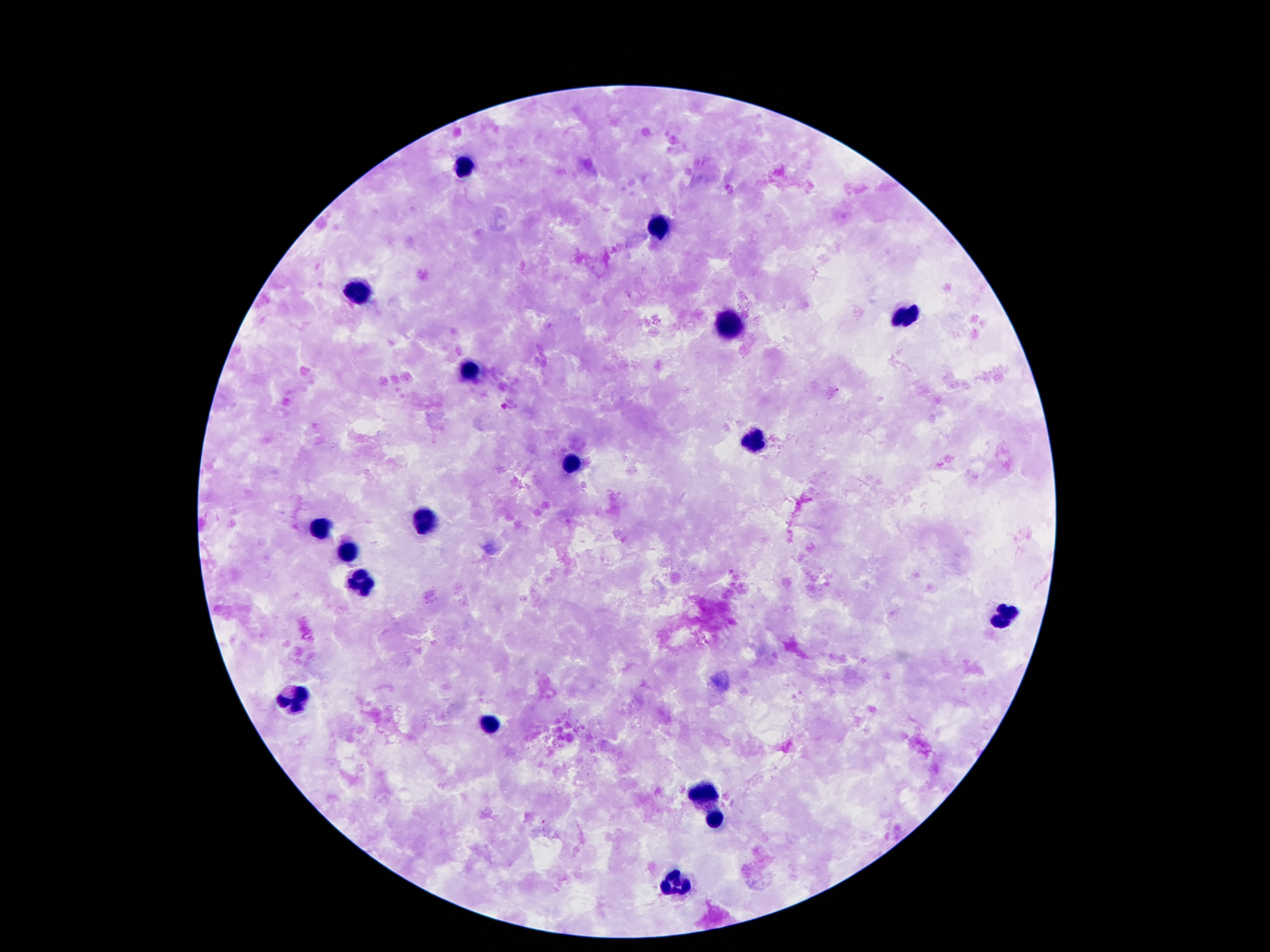

Approximate object centers, in pixels from the top-left corner.
Summary:
  - Leukocyte locations: (x=465, y=166), (x=660, y=227), (x=362, y=290), (x=905, y=317), (x=730, y=327), (x=470, y=374), (x=755, y=441), (x=571, y=465), (x=425, y=521), (x=324, y=529), (x=346, y=549), (x=359, y=586), (x=1005, y=613), (x=296, y=702), (x=486, y=724), (x=705, y=794), (x=716, y=818), (x=673, y=884)
  - Stain: Giemsa
  - Image size: 1270×952 pixels
  - Patient malaria status: negative
  - Magnification: 100x
  - Capture: smartphone camera through the microscope eyepiece
  - Preparation: thick blood smear
  - Field of view: single